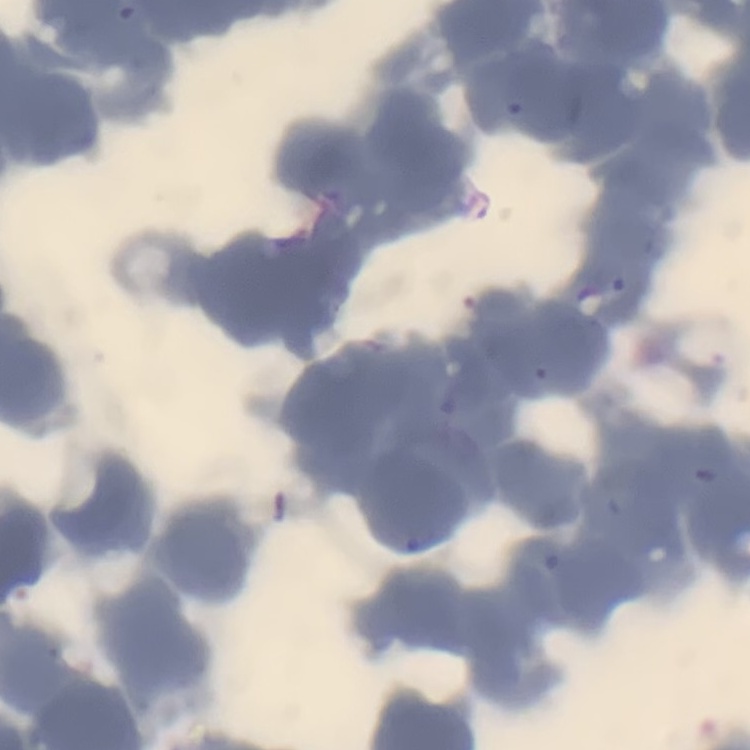
erythrocyte morphology = rouleaux formation
preparation = thin blood film
stain = Field's or Giemsa
image type = one tile cut from a larger photomicrograph